Describe the morphology of the red blood cells.
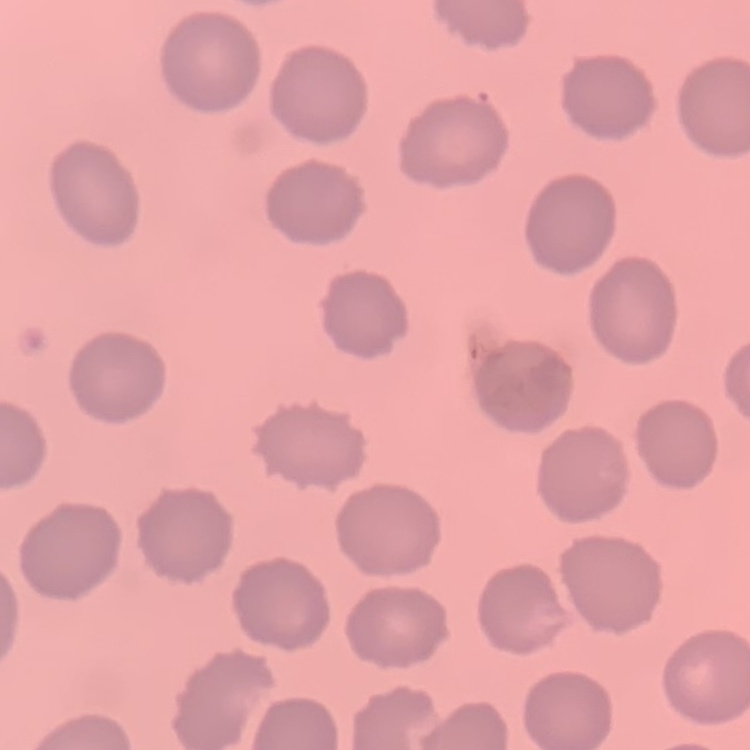

No rouleaux formation.

Summary:
  - Preparation: thin blood film
  - Stain: Field's or Giemsa
  - Image type: one tile cut from a larger photomicrograph